State which parasite is depicted.
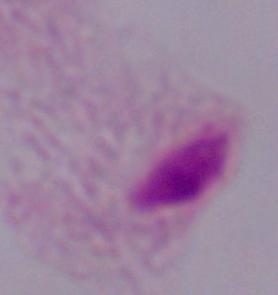
This is a trichomonad.

modality = micrograph
magnification = 1000x